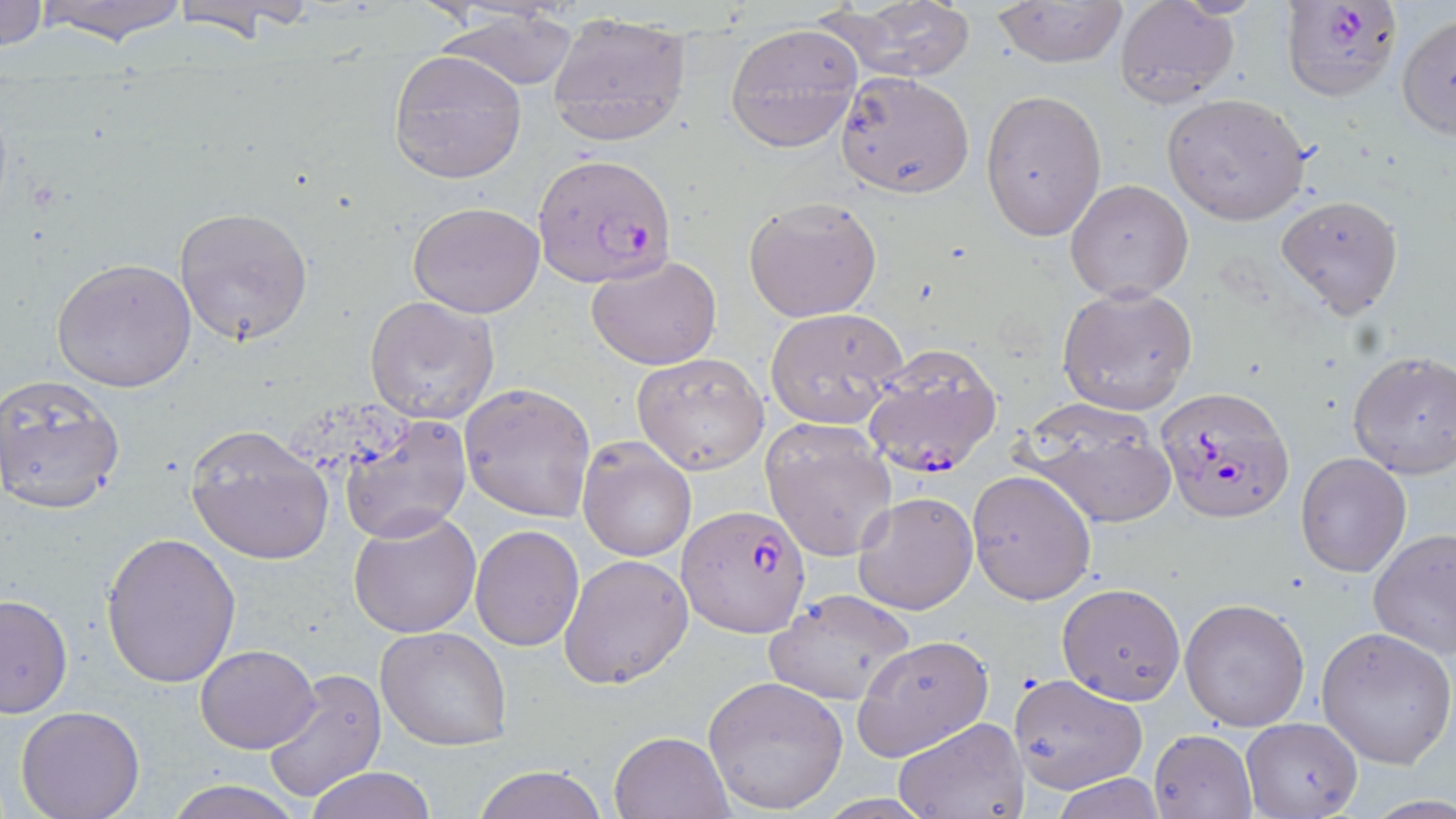

slide-level diagnosis = Plasmodium falciparum
uninfected red blood cell locations = approximate bounding boxes as (x1, y1, x2, y2) in pixels: (0, 0, 47, 53), (28, 0, 195, 45), (989, 0, 1130, 68), (168, 1, 317, 43), (1112, 1, 1240, 110), (818, 2, 979, 83), (433, 5, 583, 95), (545, 13, 694, 146), (1396, 13, 1456, 140), (725, 22, 862, 151), (388, 50, 527, 184), (832, 71, 975, 198), (980, 88, 1107, 240), (1162, 93, 1312, 225), (1066, 179, 1194, 301), (1276, 194, 1404, 319), (743, 197, 883, 322), (407, 202, 546, 318), (173, 206, 313, 344), (587, 255, 722, 370), (52, 257, 196, 394), (1058, 283, 1199, 416), (363, 296, 500, 423), (765, 307, 908, 427), (1348, 351, 1456, 479), (631, 352, 770, 475), (0, 374, 126, 515), (459, 382, 596, 524), (1016, 396, 1178, 529), (338, 414, 472, 545), (761, 420, 896, 560), (185, 423, 335, 565), (578, 439, 696, 562), (1296, 454, 1411, 577), (967, 468, 1095, 604), (854, 491, 978, 614), (348, 509, 480, 639), (470, 527, 584, 651), (1367, 528, 1456, 660), (100, 532, 242, 687), (559, 553, 694, 689), (1057, 582, 1186, 705), (764, 589, 916, 705), (0, 593, 74, 718), (1178, 597, 1310, 732), (1317, 626, 1455, 769), (376, 627, 513, 750), (852, 635, 994, 761), (194, 643, 320, 753), (260, 667, 385, 805), (1009, 673, 1148, 794), (704, 675, 848, 813), (15, 706, 146, 819), (894, 717, 1028, 818), (1241, 717, 1362, 818), (1149, 729, 1257, 818), (611, 730, 732, 818), (468, 766, 609, 819), (305, 767, 437, 819), (1050, 776, 1168, 816), (164, 778, 306, 819)
Plasmodium falciparum-infected red blood cell locations = approximate bounding boxes as (x1, y1, x2, y2) in pixels: (1280, 1, 1403, 103), (536, 161, 673, 288), (861, 345, 1005, 482), (1156, 384, 1295, 524), (676, 505, 811, 637)
field of view = single
image size = 1456×819 pixels
stain = May-Grünwald-Giemsa
magnification = 1000x
preparation = thin blood film
modality = light microscopy